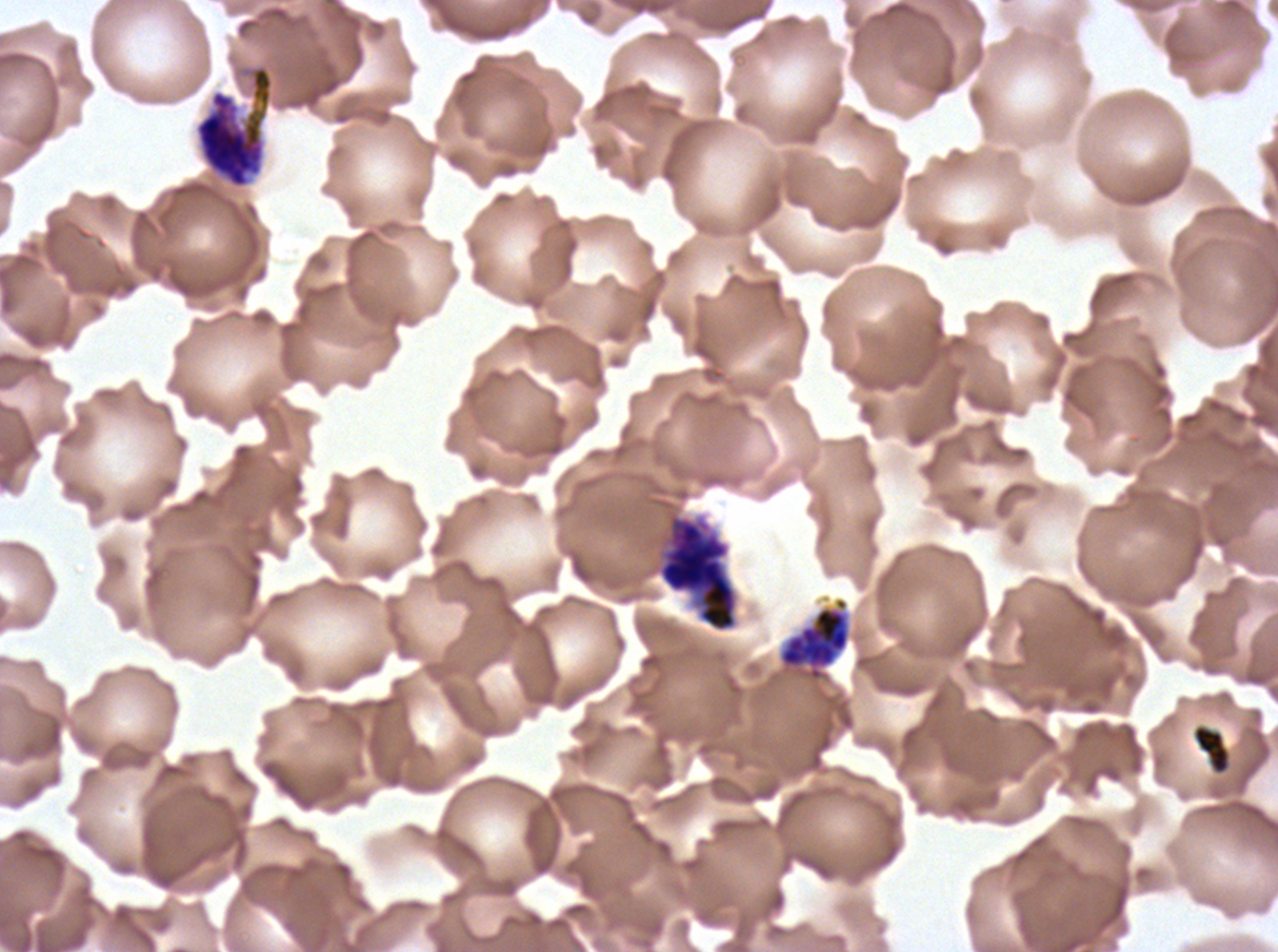

{
  "late_schizont_locations": "approximate bounding boxes as {x1, y1, x2, y2} in pixels: {194, 65, 274, 189}, {778, 597, 851, 682}",
  "debris_locations": "approximate bounding boxes as {x1, y1, x2, y2} in pixels: {1192, 724, 1231, 775}",
  "life_cycle_stages_observed": "early schizont, late schizont",
  "image_size": "1278×952 pixels",
  "field_of_view": "one sub-image of a larger composite",
  "preparation": "thin blood smear",
  "stain": "Giemsa",
  "specimen": "ex-vivo P. falciparum culture from a patient in The Gambia, grown for 24 to 48 hours",
  "early_schizont_locations": "approximate bounding boxes as {x1, y1, x2, y2} in pixels: {657, 513, 738, 632}"
}